Identify the cell.
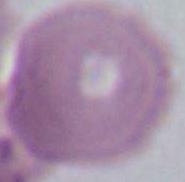
An erythrocyte.

magnification: 1000x
modality: micrograph